Classify this cell by malaria status.
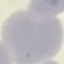
It is uninfected.

stain = Giemsa
preparation = thin blood smear
capture = smartphone camera at the microscope eyepiece
image type = cell patch, automatically extracted from a larger field of view and resized to 64 × 64 pixels